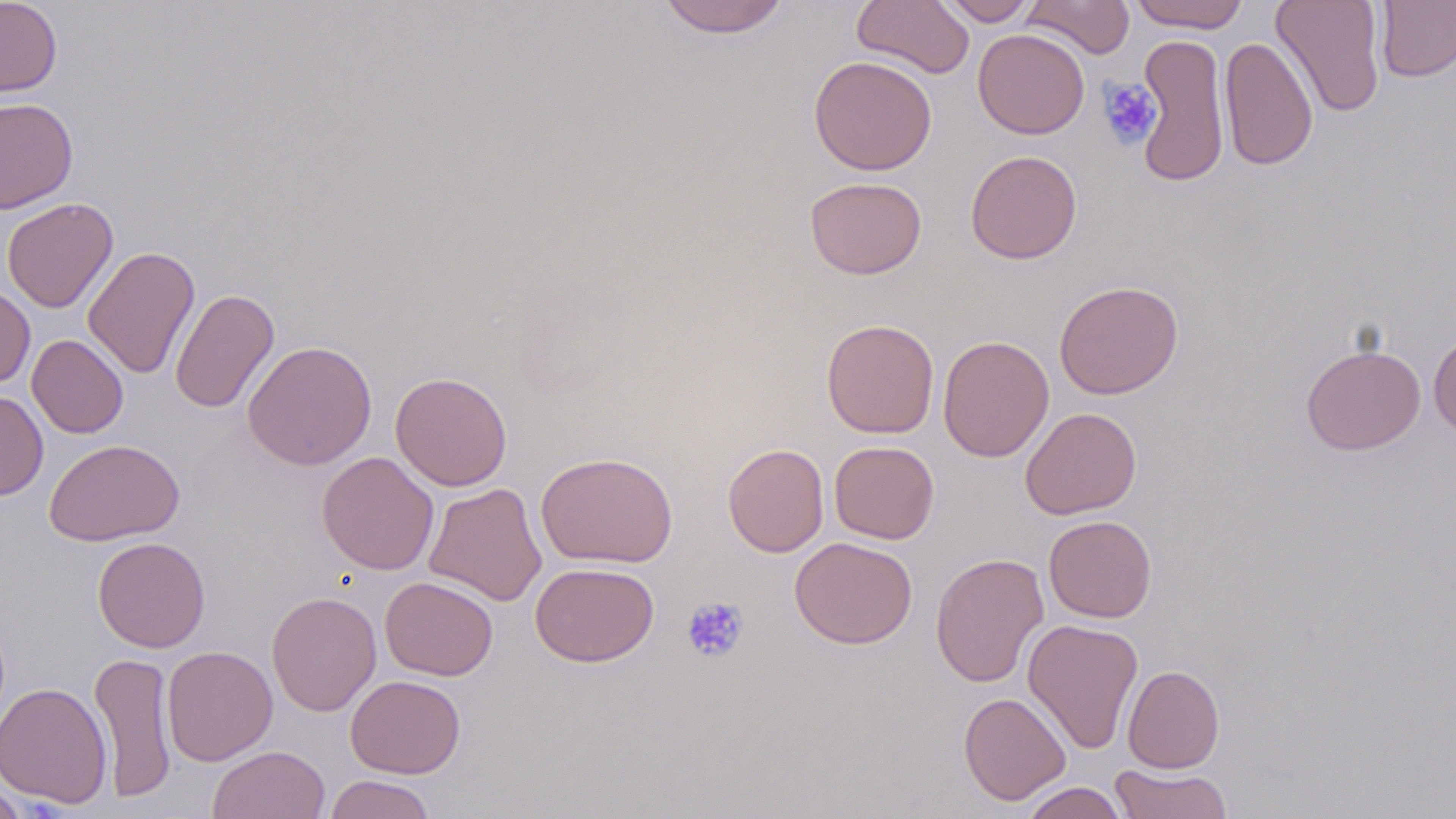

Approximate bounding boxes as named x1/y1/x2/y2 corners in pixels. Platelet locations: (x1=1097, y1=78, x2=1162, y2=148), (x1=682, y1=597, x2=749, y2=663). Uninfected red blood cell locations: (x1=0, y1=0, x2=62, y2=97), (x1=658, y1=0, x2=790, y2=38), (x1=851, y1=0, x2=975, y2=79), (x1=936, y1=0, x2=1039, y2=26), (x1=1022, y1=0, x2=1135, y2=59), (x1=1128, y1=0, x2=1251, y2=32), (x1=1271, y1=0, x2=1386, y2=117), (x1=1375, y1=1, x2=1456, y2=82), (x1=972, y1=28, x2=1090, y2=139), (x1=1134, y1=33, x2=1230, y2=188), (x1=1218, y1=37, x2=1318, y2=170), (x1=809, y1=55, x2=937, y2=176), (x1=0, y1=97, x2=78, y2=213), (x1=965, y1=149, x2=1082, y2=264), (x1=805, y1=177, x2=927, y2=279), (x1=2, y1=198, x2=119, y2=313), (x1=83, y1=245, x2=200, y2=379), (x1=1054, y1=280, x2=1183, y2=399), (x1=0, y1=282, x2=35, y2=388), (x1=169, y1=287, x2=279, y2=414), (x1=822, y1=318, x2=939, y2=438), (x1=1428, y1=332, x2=1456, y2=438), (x1=27, y1=334, x2=129, y2=438), (x1=937, y1=335, x2=1054, y2=462), (x1=242, y1=340, x2=377, y2=470), (x1=1301, y1=343, x2=1425, y2=455), (x1=390, y1=372, x2=512, y2=491), (x1=0, y1=390, x2=49, y2=500), (x1=1020, y1=406, x2=1142, y2=520), (x1=44, y1=439, x2=184, y2=546), (x1=828, y1=440, x2=940, y2=544), (x1=723, y1=443, x2=829, y2=557), (x1=317, y1=451, x2=439, y2=575), (x1=535, y1=451, x2=678, y2=568), (x1=424, y1=483, x2=547, y2=606), (x1=1043, y1=515, x2=1157, y2=622), (x1=93, y1=537, x2=210, y2=653), (x1=790, y1=537, x2=918, y2=649), (x1=930, y1=552, x2=1049, y2=688), (x1=530, y1=562, x2=659, y2=667), (x1=380, y1=576, x2=498, y2=681), (x1=266, y1=591, x2=381, y2=717), (x1=1023, y1=618, x2=1144, y2=755), (x1=161, y1=645, x2=277, y2=766), (x1=90, y1=650, x2=177, y2=802), (x1=1122, y1=665, x2=1225, y2=773), (x1=345, y1=675, x2=465, y2=778), (x1=0, y1=682, x2=113, y2=808), (x1=958, y1=692, x2=1071, y2=805), (x1=208, y1=745, x2=330, y2=819), (x1=1109, y1=764, x2=1233, y2=818), (x1=324, y1=774, x2=436, y2=819), (x1=0, y1=779, x2=29, y2=819), (x1=1020, y1=782, x2=1128, y2=819). Slide-level diagnosis: no evidence of blood parasites. May-Grünwald-Giemsa-stained preparation. Image is 1456×819 pixels. Captured at 1000x magnification. Thin blood film. Optical microscopy. One field of a larger specimen.